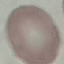
Result: no malaria parasites seen. Thin blood film. Acquired by smartphone through the microscope eyepiece. Giemsa-stained preparation. Automatically extracted cell patch, resized to 64 × 64 pixels.